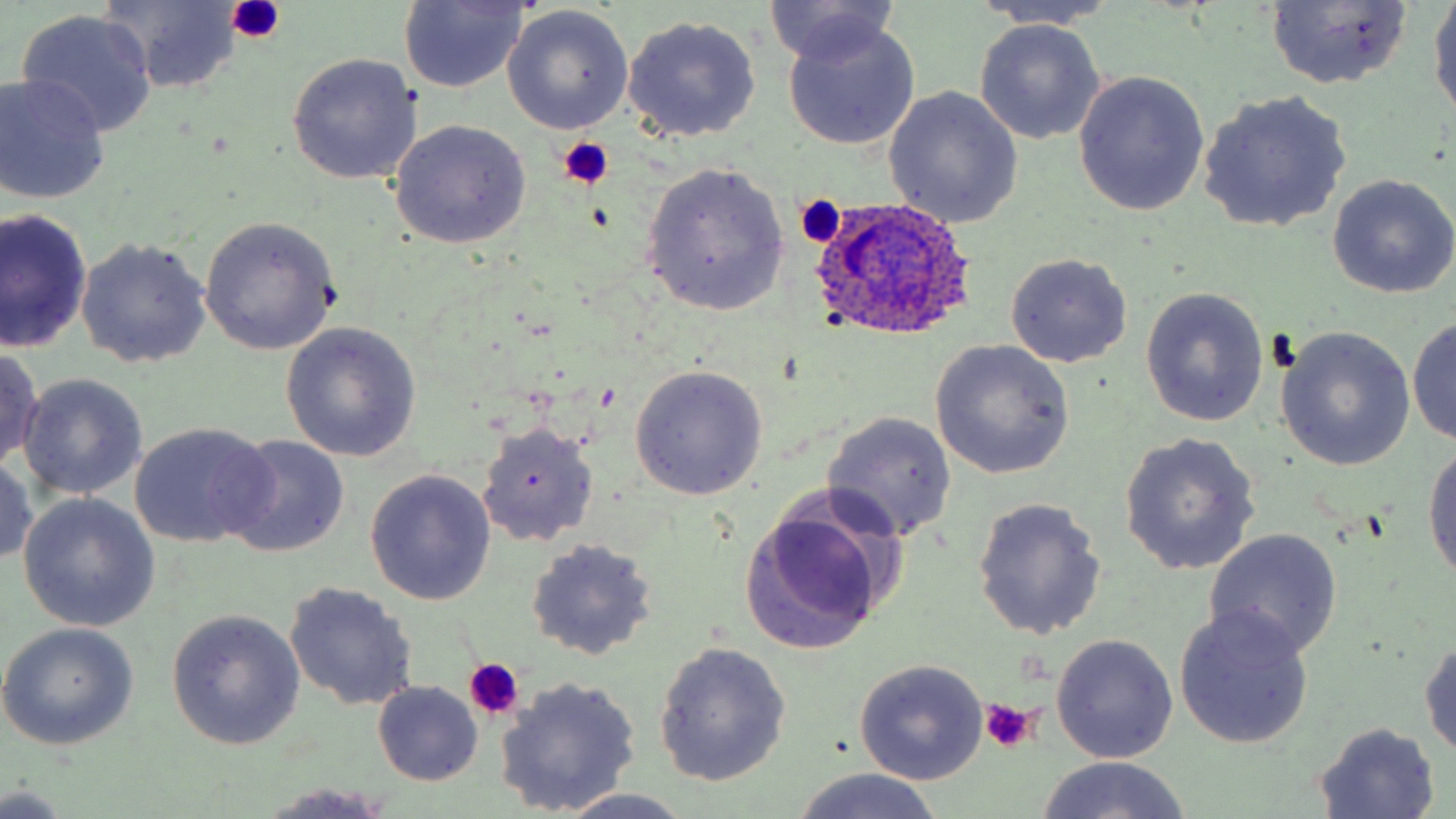

Summary:
  - Coordinate format: approximate bounding boxes as (x1,y1)-(x2,y2) corner pairs in pixels
  - Uninfected red blood cell locations: (1429,0)-(1456,121), (398,1)-(529,93), (765,1)-(904,70), (98,2)-(248,90), (971,2)-(1121,31), (1265,2)-(1413,90), (504,7)-(635,134), (17,10)-(157,136), (621,14)-(762,142), (781,16)-(921,152), (975,19)-(1106,144), (286,53)-(422,186), (1072,72)-(1208,216), (0,73)-(112,204), (882,87)-(1024,229), (1199,90)-(1354,234), (388,119)-(531,249), (640,161)-(791,315), (1326,174)-(1456,299), (1,210)-(92,352), (198,217)-(340,354), (76,237)-(211,368), (1004,253)-(1133,368), (1141,287)-(1269,428), (1408,316)-(1456,445), (280,322)-(422,462), (1274,327)-(1416,472), (930,340)-(1074,479), (0,347)-(45,470), (629,365)-(768,500), (18,374)-(147,501), (822,412)-(957,542), (130,422)-(276,548), (476,422)-(599,547), (1119,433)-(1261,575), (221,436)-(351,557), (1422,439)-(1456,595), (0,452)-(38,568), (365,470)-(497,606), (19,494)-(158,632), (971,497)-(1107,639), (739,501)-(895,654), (1204,527)-(1344,659), (526,538)-(658,660), (285,582)-(419,711), (1173,604)-(1316,750), (167,611)-(304,749), (0,623)-(140,751), (1051,634)-(1179,763), (1419,635)-(1456,765), (655,641)-(791,785), (853,661)-(988,785), (495,675)-(643,816), (373,682)-(482,785), (1312,723)-(1443,816), (1035,756)-(1194,819), (789,768)-(947,819), (260,784)-(398,817), (0,785)-(72,816), (548,790)-(699,819)
  - Platelet locations: (226,0)-(287,42), (558,137)-(615,190), (796,193)-(847,248), (463,659)-(526,721), (977,700)-(1042,756)
  - Plasmodium ovale-infected red blood cell locations: (809,196)-(977,341)
  - Slide-level diagnosis: Plasmodium ovale
  - Modality: light microscopy
  - Image size: 1456×819 pixels
  - Magnification: 1000x
  - Preparation: thin blood film
  - Field of view: one of a larger specimen
  - Stain: May-Grünwald-Giemsa